Comment on the morphology of the red blood cells.
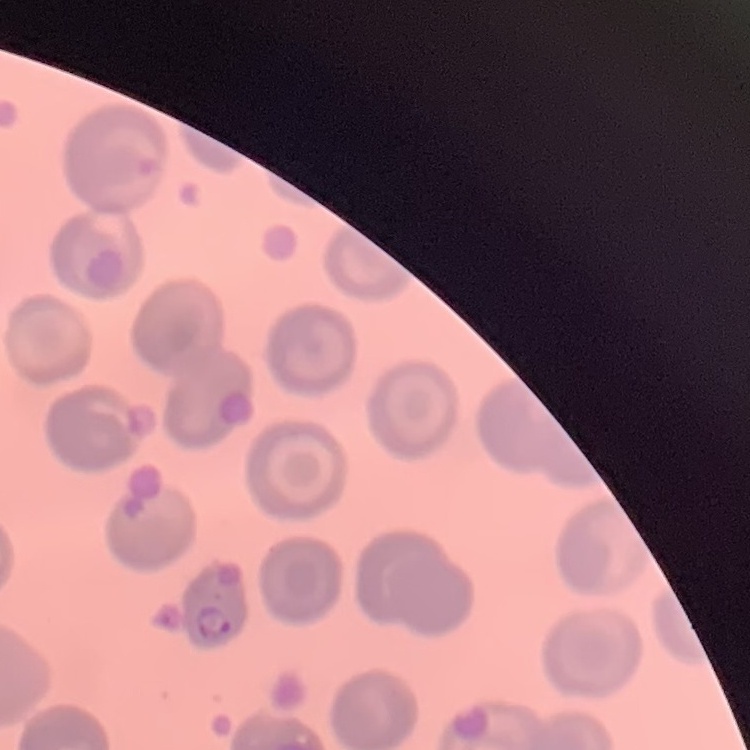

They show no rouleaux formation.

preparation = thin blood smear
stain = Field's or Giemsa
image type = one tile cut from a larger photomicrograph